Assess the morphology of the erythrocytes.
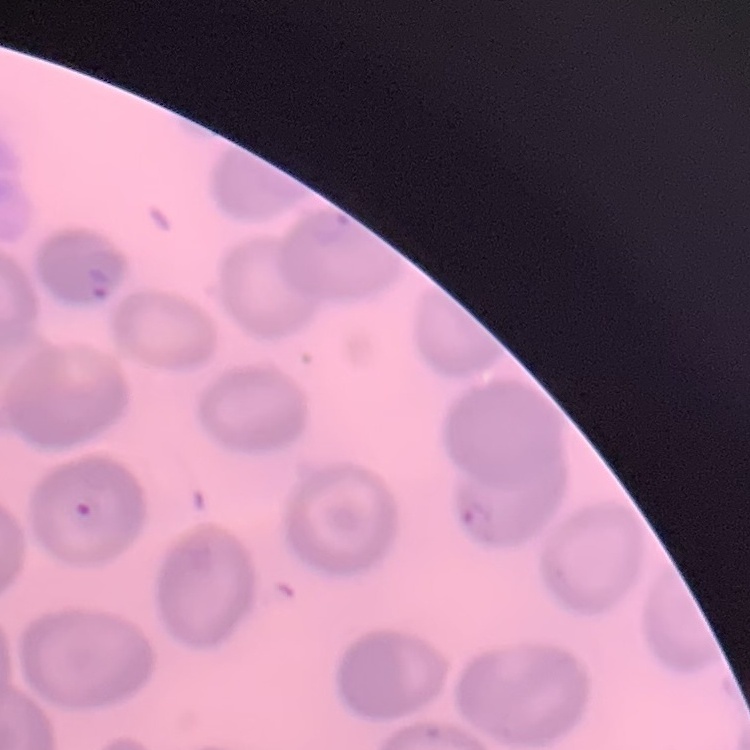
They show no rouleaux formation.

image type = square crop of a larger photomicrograph
preparation = thin blood film
stain = Field's or Giemsa